Locate and identify every blood parasite.
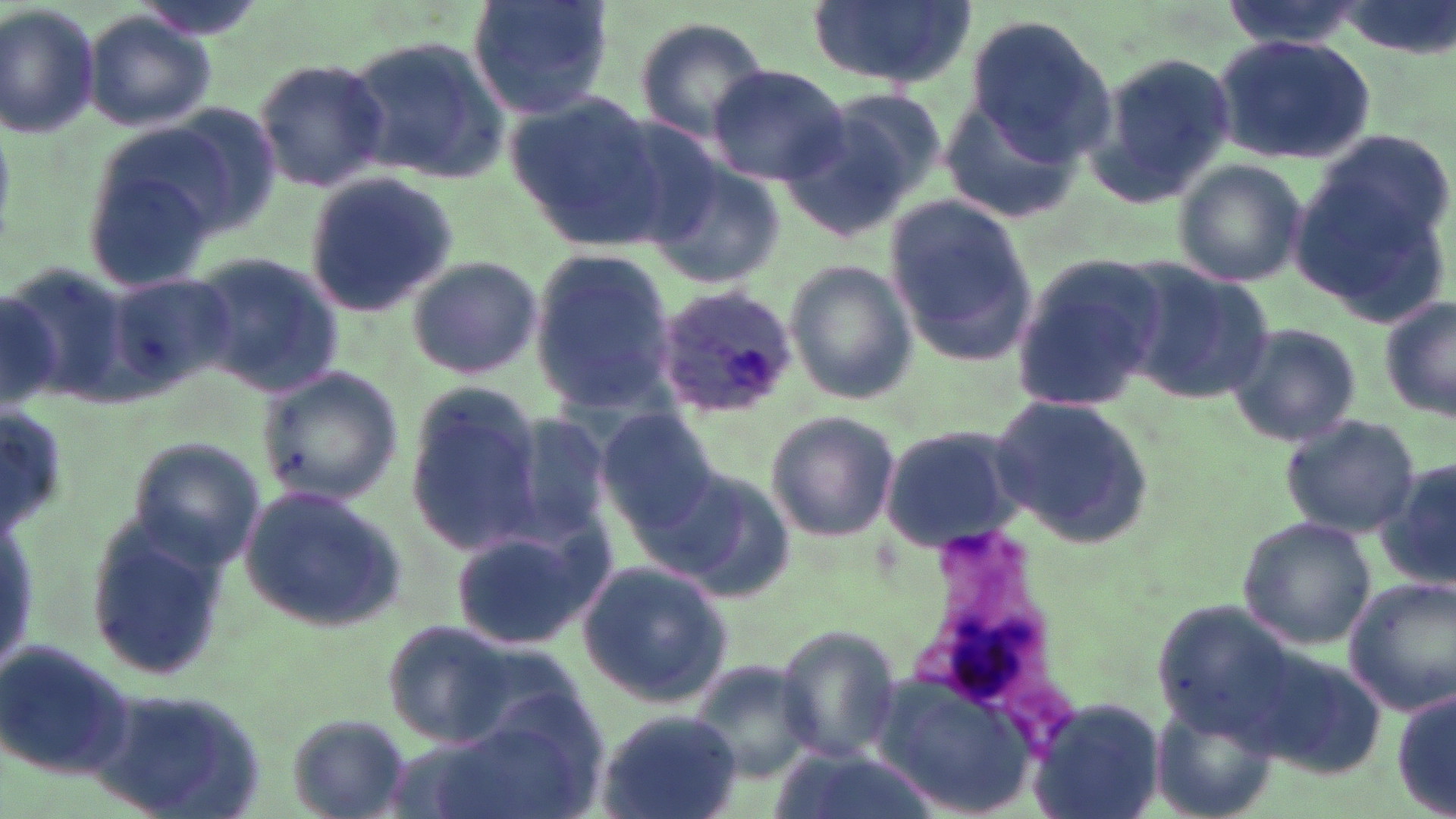

Approximate bounding boxes as (x1,y1)-(x2,y2) corner pairs in pixels.
Plasmodium ovale-infected red blood cells: (649,283)-(799,423).
No Plasmodium falciparum, Plasmodium malariae, Plasmodium vivax, Babesia divergens, or Trypanosoma brucei observed.

slide-level diagnosis = Plasmodium ovale
modality = optical microscopy
uninfected red blood cell locations = approximate bounding boxes as (x1,y1)-(x2,y2) corner pairs in pixels: (466,0)-(616,118), (1333,0)-(1453,57), (807,1)-(975,91), (0,2)-(102,141), (82,11)-(216,133), (959,13)-(1113,163), (631,16)-(771,148), (345,33)-(507,180), (1212,33)-(1375,165), (1087,49)-(1236,209), (252,57)-(389,193), (706,64)-(851,186), (824,86)-(950,200), (505,89)-(663,240), (941,98)-(1083,223), (782,107)-(926,238), (1296,134)-(1453,317), (78,138)-(232,292), (645,154)-(786,288), (1169,159)-(1306,288), (302,172)-(455,319), (884,196)-(1035,364), (529,248)-(681,416), (188,250)-(343,398), (407,254)-(543,381), (1010,255)-(1167,414), (784,258)-(919,404), (1121,264)-(1275,404), (106,271)-(234,399), (0,276)-(83,408), (1379,297)-(1456,424), (1224,321)-(1362,449), (255,365)-(403,508), (403,387)-(547,558), (989,396)-(1156,547), (595,408)-(722,530), (763,410)-(899,542), (497,413)-(619,545), (1278,414)-(1421,539), (878,421)-(1030,552), (121,438)-(265,574), (1376,456)-(1456,592), (643,461)-(794,601), (237,485)-(408,635), (1238,515)-(1375,649), (449,521)-(613,650), (81,523)-(230,681), (575,558)-(733,706), (1344,576)-(1455,717), (386,619)-(513,745), (771,625)-(904,766), (0,639)-(133,782), (688,661)-(824,781), (873,670)-(1039,818), (1391,682)-(1455,818), (1024,695)-(1167,819), (1151,698)-(1278,812), (592,709)-(745,819), (284,715)-(412,817)
image size = 1456×819 pixels
stain = May-Grünwald-Giemsa
preparation = thin blood smear
magnification = 1000x
field of view = one of a larger specimen